Mark where platelets are.
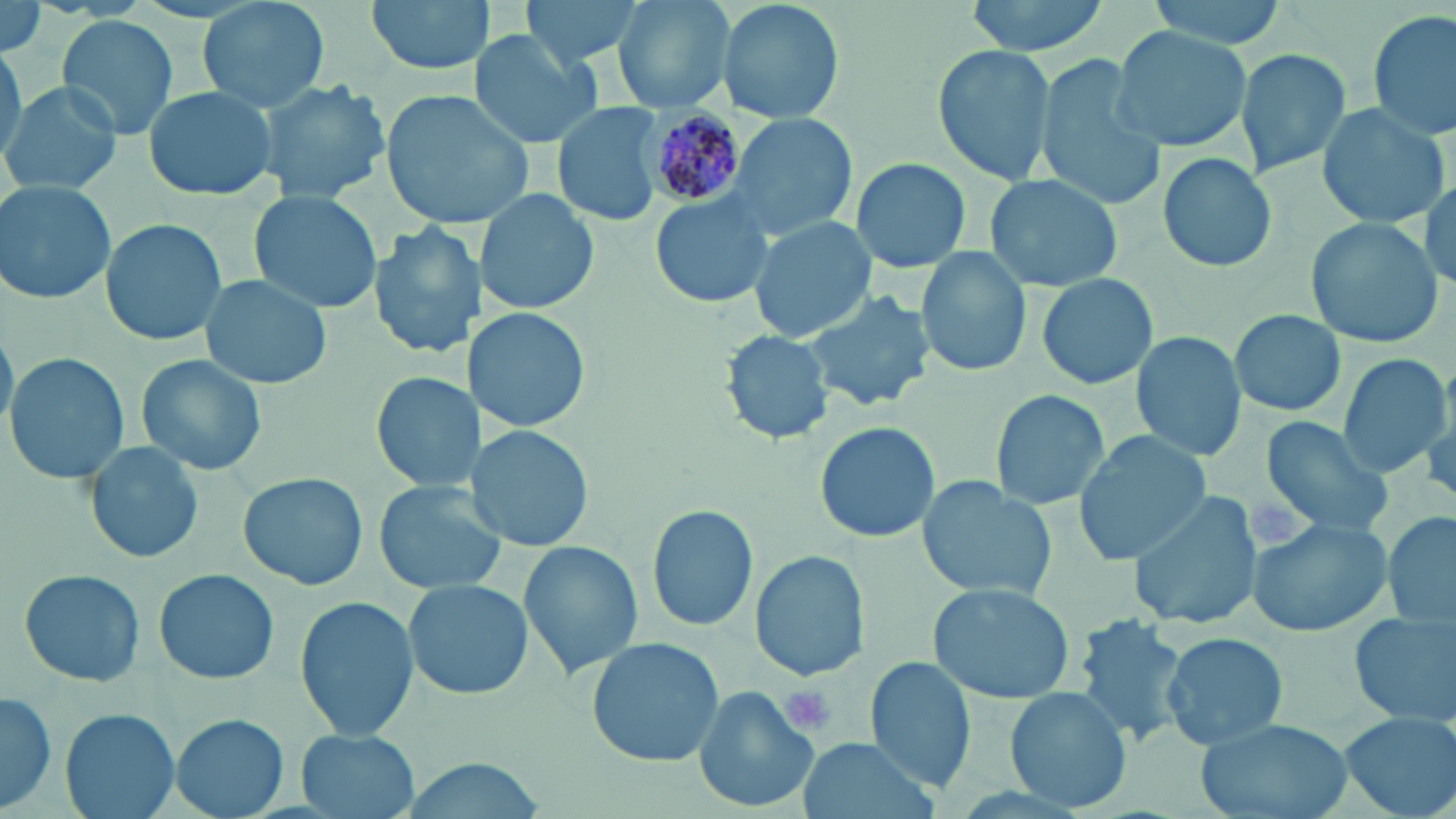

Approximate bounding boxes as named x1/y1/x2/y2 corners in pixels.
Platelets: (x1=781, y1=684, x2=836, y2=736).

slide_level_diagnosis: Plasmodium malariae
uninfected_red_blood_cell_locations: 'approximate bounding boxes as named x1/y1/x2/y2 corners in pixels: (x1=198, y1=0, x2=331, y2=111), (x1=366, y1=0, x2=496, y2=78), (x1=521, y1=0, x2=649, y2=67), (x1=615, y1=0, x2=737, y2=113), (x1=719, y1=0, x2=844, y2=122), (x1=962, y1=0, x2=1109, y2=55), (x1=1145, y1=0, x2=1286, y2=46), (x1=1, y1=2, x2=47, y2=61), (x1=1369, y1=9, x2=1455, y2=142), (x1=58, y1=14, x2=180, y2=140), (x1=1110, y1=26, x2=1251, y2=153), (x1=470, y1=30, x2=606, y2=148), (x1=0, y1=42, x2=27, y2=163), (x1=933, y1=45, x2=1056, y2=184), (x1=1236, y1=48, x2=1351, y2=177), (x1=1035, y1=56, x2=1169, y2=213), (x1=254, y1=78, x2=390, y2=205), (x1=1, y1=80, x2=123, y2=195), (x1=143, y1=84, x2=282, y2=201), (x1=378, y1=88, x2=536, y2=229), (x1=552, y1=102, x2=666, y2=228), (x1=1316, y1=103, x2=1450, y2=228), (x1=725, y1=112, x2=852, y2=241), (x1=1158, y1=152, x2=1277, y2=273), (x1=852, y1=157, x2=971, y2=275), (x1=985, y1=174, x2=1123, y2=292), (x1=1, y1=181, x2=117, y2=305), (x1=478, y1=189, x2=596, y2=317), (x1=250, y1=190, x2=380, y2=316), (x1=650, y1=191, x2=771, y2=305), (x1=100, y1=217, x2=226, y2=347), (x1=1304, y1=217, x2=1442, y2=351), (x1=748, y1=218, x2=876, y2=343), (x1=367, y1=221, x2=481, y2=361), (x1=916, y1=248, x2=1031, y2=378), (x1=199, y1=273, x2=333, y2=390), (x1=1037, y1=273, x2=1159, y2=391), (x1=802, y1=288, x2=933, y2=411), (x1=474, y1=308, x2=591, y2=431), (x1=1229, y1=309, x2=1347, y2=417), (x1=722, y1=329, x2=836, y2=445), (x1=1130, y1=330, x2=1247, y2=465), (x1=6, y1=350, x2=129, y2=484), (x1=135, y1=353, x2=267, y2=477), (x1=1338, y1=353, x2=1449, y2=474), (x1=371, y1=371, x2=475, y2=492), (x1=989, y1=389, x2=1109, y2=511), (x1=1259, y1=416, x2=1393, y2=536), (x1=813, y1=421, x2=941, y2=543), (x1=471, y1=425, x2=596, y2=552), (x1=1074, y1=433, x2=1210, y2=564), (x1=83, y1=438, x2=206, y2=566), (x1=237, y1=472, x2=366, y2=590), (x1=917, y1=477, x2=1061, y2=603), (x1=375, y1=481, x2=507, y2=597), (x1=1127, y1=489, x2=1264, y2=630), (x1=646, y1=503, x2=758, y2=633), (x1=1383, y1=508, x2=1456, y2=635), (x1=1245, y1=514, x2=1395, y2=639), (x1=518, y1=537, x2=644, y2=679), (x1=751, y1=550, x2=871, y2=682), (x1=151, y1=567, x2=280, y2=685), (x1=18, y1=568, x2=145, y2=687), (x1=405, y1=578, x2=532, y2=700), (x1=927, y1=581, x2=1076, y2=704), (x1=295, y1=596, x2=418, y2=741), (x1=1350, y1=613, x2=1454, y2=728), (x1=1071, y1=615, x2=1190, y2=745), (x1=1161, y1=631, x2=1289, y2=751), (x1=588, y1=637, x2=724, y2=766), (x1=868, y1=657, x2=977, y2=794), (x1=1004, y1=684, x2=1133, y2=812), (x1=694, y1=687, x2=817, y2=812), (x1=1, y1=689, x2=58, y2=812), (x1=61, y1=708, x2=180, y2=819), (x1=1338, y1=711, x2=1456, y2=819), (x1=170, y1=713, x2=289, y2=818), (x1=1194, y1=715, x2=1355, y2=819), (x1=296, y1=729, x2=419, y2=819), (x1=796, y1=735, x2=940, y2=819)'
modality: light microscopy
stain: May-Grünwald-Giemsa
plasmodium_malariae_infected_red_blood_cell_locations: 'approximate bounding boxes as named x1/y1/x2/y2 corners in pixels: (x1=630, y1=99, x2=751, y2=212)'
image_size: 1456×819 pixels
magnification: 1000x
preparation: thin blood smear
field_of_view: single